Give the position of every Plasmodium parasite visible.
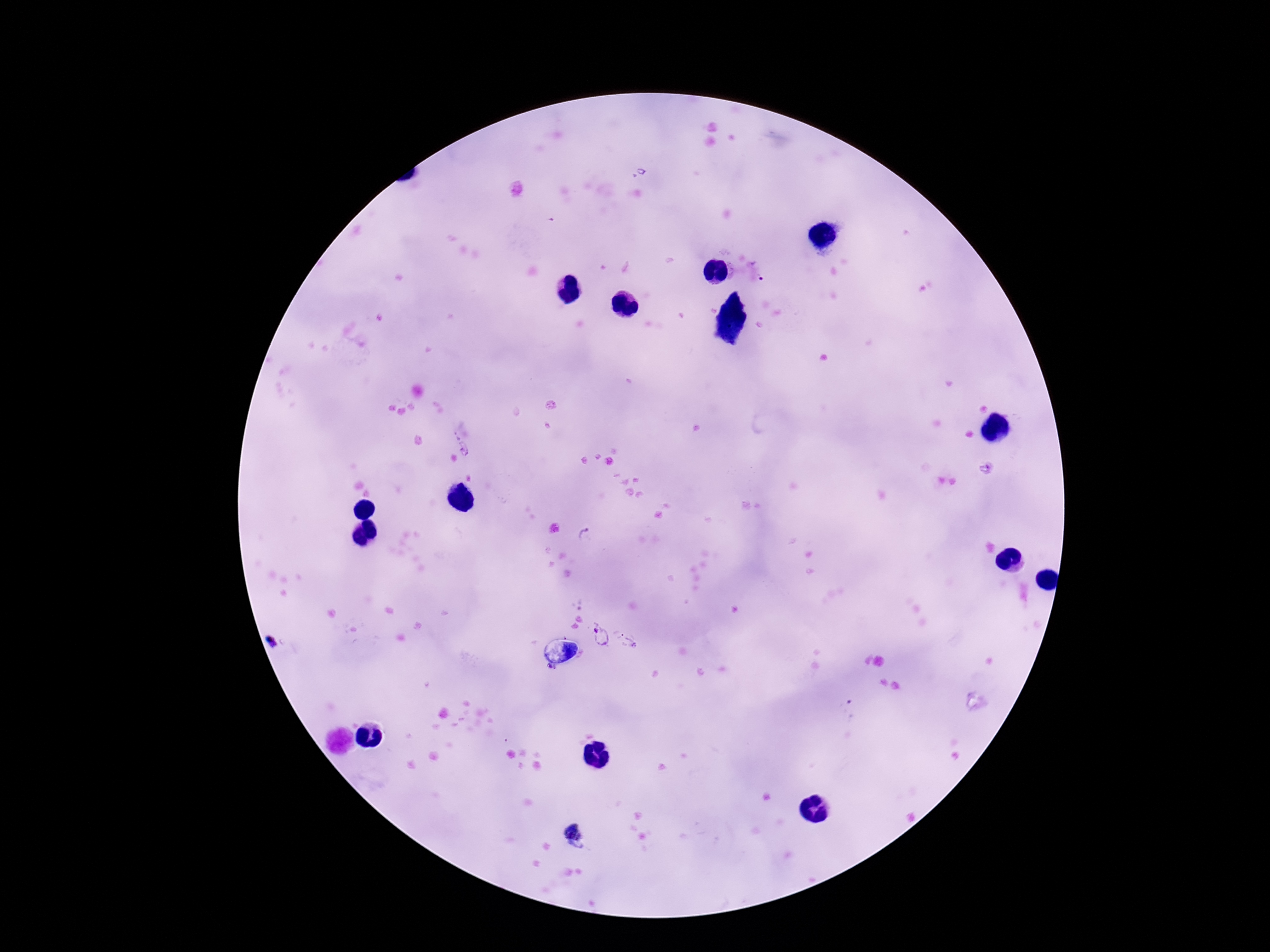
Approximate centers as [x, y] in pixels.
Plasmodium parasites: [761, 270], [986, 468], [588, 537], [600, 638], [276, 640], [628, 642], [549, 667], [849, 711], [575, 836].

Summary:
  - Magnification: 100x
  - Field of view: one from this slide
  - Patient malaria status: positive
  - Preparation: thick blood film
  - Capture: smartphone camera through the microscope eyepiece
  - Stain: Giemsa
  - Image size: 1270×952 pixels